Give a bounding box for every malaria parasite.
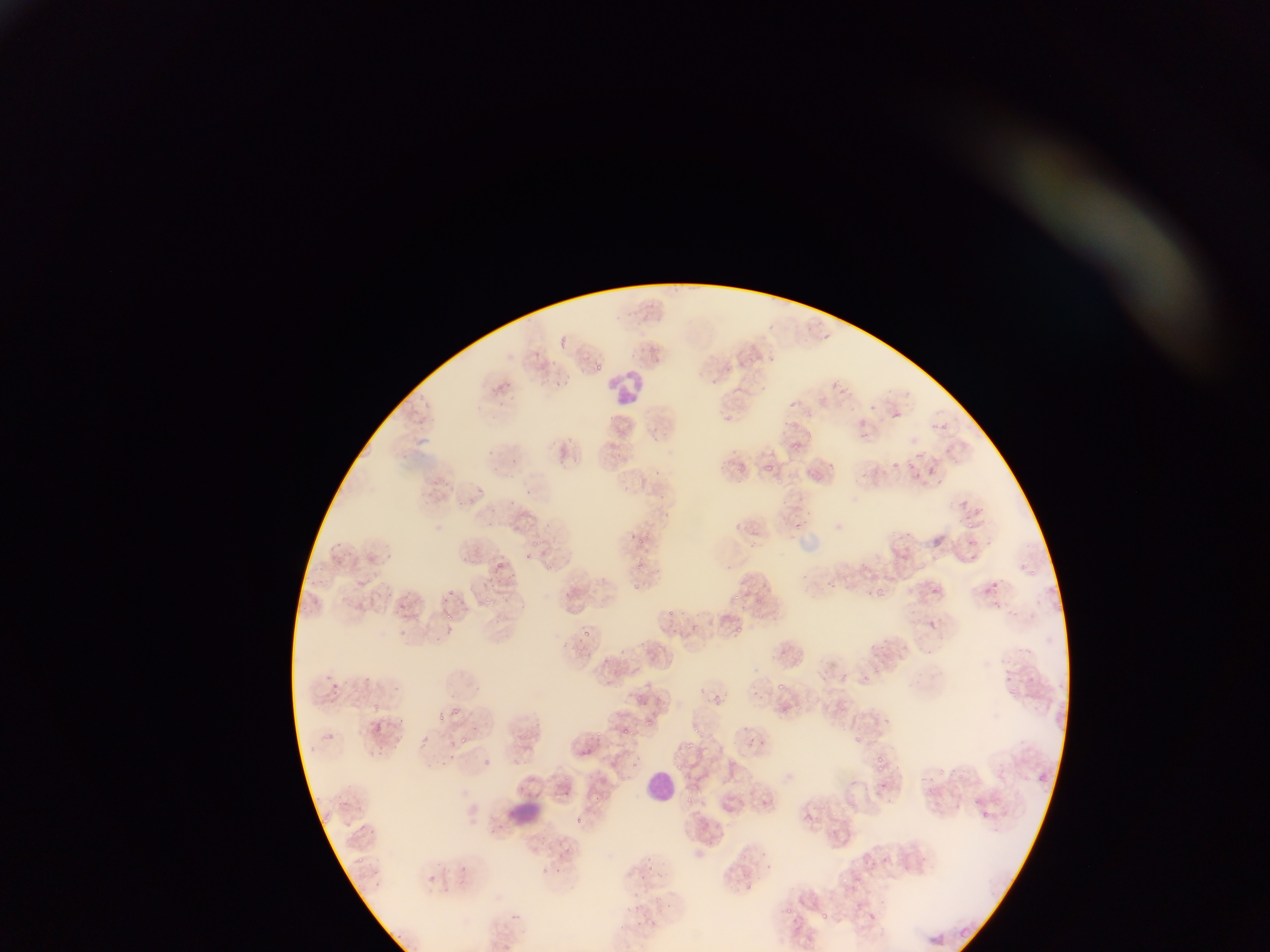

Approximate bounding boxes as left top right bottom in pixels.
Malaria parasites: 598 359 606 372; 552 379 561 387; 830 381 839 388; 789 400 798 409; 869 402 877 411; 893 410 906 421; 936 419 954 433; 806 430 811 438; 793 441 800 452; 913 450 926 458; 766 460 774 473; 891 460 897 468; 928 466 939 478; 476 485 485 495; 961 500 970 509; 965 519 977 530; 797 521 802 529; 638 537 648 546; 524 551 534 561; 894 554 905 565; 495 563 506 571; 485 576 496 587; 826 577 843 591; 876 582 889 593; 991 582 999 591; 447 587 457 596; 932 587 941 597; 564 591 572 598; 730 593 743 605; 380 594 388 607; 482 594 492 608; 397 599 405 610; 444 606 452 618; 666 610 676 617; 734 625 744 635; 582 627 592 637; 868 663 881 671; 324 673 334 686; 863 673 876 684; 777 678 787 690; 714 696 724 705; 372 702 379 711; 436 710 444 719; 644 715 655 725; 374 723 384 734; 617 724 631 734; 742 724 751 732; 692 726 703 736; 856 735 865 745; 444 736 454 747; 686 742 698 750; 378 743 386 756; 676 743 683 751; 876 754 882 764; 631 757 642 769; 675 764 686 774; 881 780 891 793; 681 794 699 809; 846 801 854 812; 982 811 989 819; 805 813 814 822; 578 819 585 831; 647 864 655 873; 781 906 795 918; 820 909 833 925; 867 911 881 922; 961 922 971 948 | approximate x y pixel centers of objects too small to bound: 827 336; 632 538; 635 588; 402 633; 336 684; 464 738; 360 859.

Leukocyte locations: 612 371 644 407; 647 769 679 803; 504 799 551 826. Photographed through a microscope with a mobile-phone camera. Collected in Ghana. Thin blood film. One field of view. Image is 1270×952 pixels.